Describe the morphology of the erythrocytes.
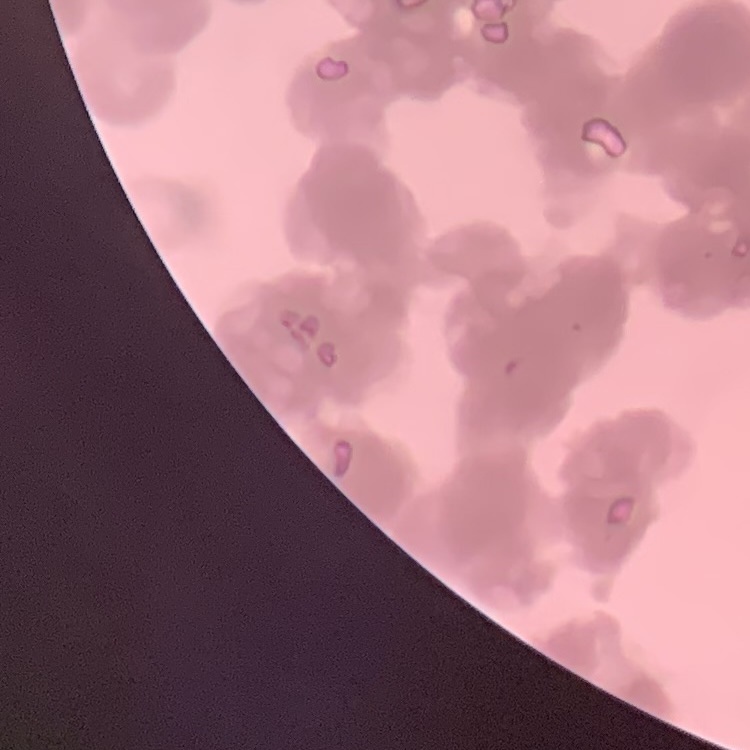

They show rouleaux formation.

image_type: square crop of a larger photomicrograph
preparation: thin peripheral smear
stain: Field's or Giemsa